Give the extent of all Plasmodium falciparum-infected red blood cells.
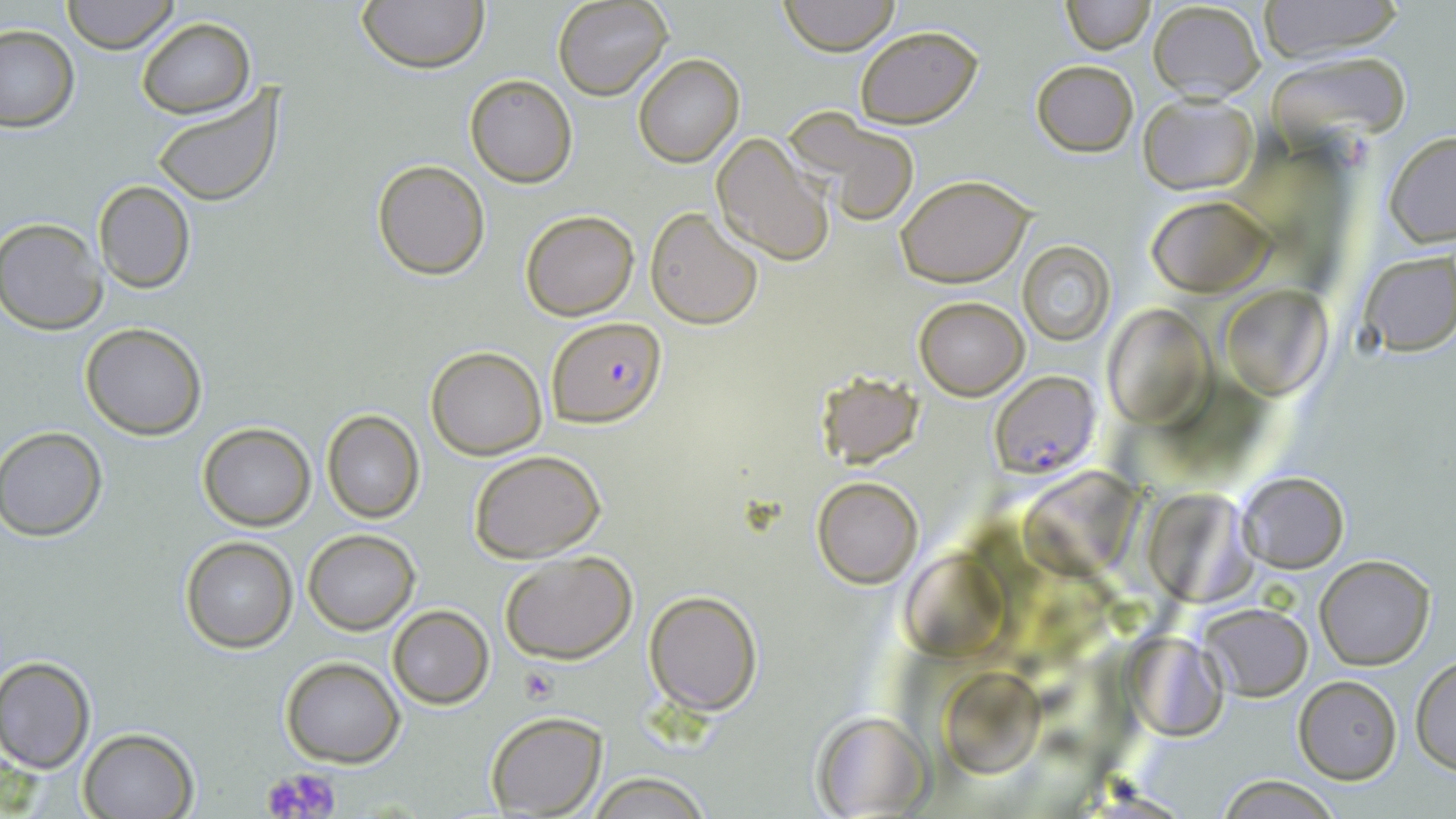

Approximate bounding boxes as named x1/y1/x2/y2 corners in pixels.
Plasmodium falciparum-infected red blood cells: (x1=548, y1=316, x2=666, y2=426), (x1=990, y1=370, x2=1098, y2=478).

Summary:
  - Uninfected red blood cell locations: (x1=63, y1=0, x2=178, y2=53), (x1=358, y1=0, x2=489, y2=73), (x1=552, y1=0, x2=672, y2=100), (x1=779, y1=0, x2=900, y2=53), (x1=1061, y1=0, x2=1153, y2=53), (x1=1147, y1=1, x2=1268, y2=102), (x1=1260, y1=1, x2=1403, y2=61), (x1=135, y1=18, x2=254, y2=118), (x1=0, y1=24, x2=79, y2=132), (x1=854, y1=25, x2=983, y2=128), (x1=1264, y1=50, x2=1412, y2=144), (x1=633, y1=55, x2=743, y2=168), (x1=1030, y1=60, x2=1140, y2=156), (x1=463, y1=73, x2=577, y2=187), (x1=151, y1=85, x2=287, y2=208), (x1=1137, y1=92, x2=1259, y2=195), (x1=785, y1=112, x2=921, y2=228), (x1=1384, y1=131, x2=1456, y2=245), (x1=710, y1=133, x2=835, y2=267), (x1=372, y1=159, x2=490, y2=279), (x1=896, y1=174, x2=1034, y2=286), (x1=93, y1=180, x2=195, y2=294), (x1=1149, y1=194, x2=1273, y2=295), (x1=645, y1=208, x2=763, y2=330), (x1=519, y1=210, x2=638, y2=320), (x1=1, y1=216, x2=109, y2=334), (x1=1016, y1=241, x2=1115, y2=347), (x1=1355, y1=250, x2=1456, y2=356), (x1=1222, y1=286, x2=1330, y2=398), (x1=914, y1=296, x2=1028, y2=400), (x1=1100, y1=303, x2=1210, y2=424), (x1=80, y1=322, x2=207, y2=439), (x1=426, y1=346, x2=546, y2=458), (x1=814, y1=371, x2=922, y2=468), (x1=321, y1=411, x2=423, y2=524), (x1=197, y1=424, x2=315, y2=530), (x1=0, y1=427, x2=106, y2=539), (x1=469, y1=449, x2=606, y2=563), (x1=1022, y1=469, x2=1140, y2=572), (x1=1237, y1=471, x2=1348, y2=571), (x1=811, y1=475, x2=924, y2=588), (x1=1148, y1=490, x2=1262, y2=603), (x1=302, y1=529, x2=419, y2=634), (x1=180, y1=536, x2=298, y2=653), (x1=500, y1=549, x2=638, y2=664), (x1=896, y1=553, x2=1014, y2=655), (x1=1315, y1=554, x2=1436, y2=670), (x1=644, y1=590, x2=762, y2=714), (x1=1196, y1=602, x2=1311, y2=700), (x1=388, y1=606, x2=494, y2=709), (x1=1123, y1=629, x2=1225, y2=735), (x1=1412, y1=655, x2=1456, y2=775), (x1=0, y1=656, x2=96, y2=772), (x1=280, y1=656, x2=405, y2=768), (x1=942, y1=667, x2=1043, y2=774), (x1=1293, y1=676, x2=1401, y2=783), (x1=483, y1=711, x2=607, y2=817), (x1=811, y1=711, x2=932, y2=818), (x1=78, y1=727, x2=198, y2=819), (x1=585, y1=770, x2=712, y2=818), (x1=1218, y1=774, x2=1339, y2=818)
  - Platelet locations: (x1=521, y1=667, x2=556, y2=703), (x1=261, y1=766, x2=340, y2=819)
  - Slide-level diagnosis: Plasmodium falciparum
  - Stain: May-Grünwald-Giemsa
  - Field of view: one of a larger specimen
  - Modality: light microscopy
  - Magnification: 1000x
  - Image size: 1456×819 pixels
  - Preparation: thin blood film